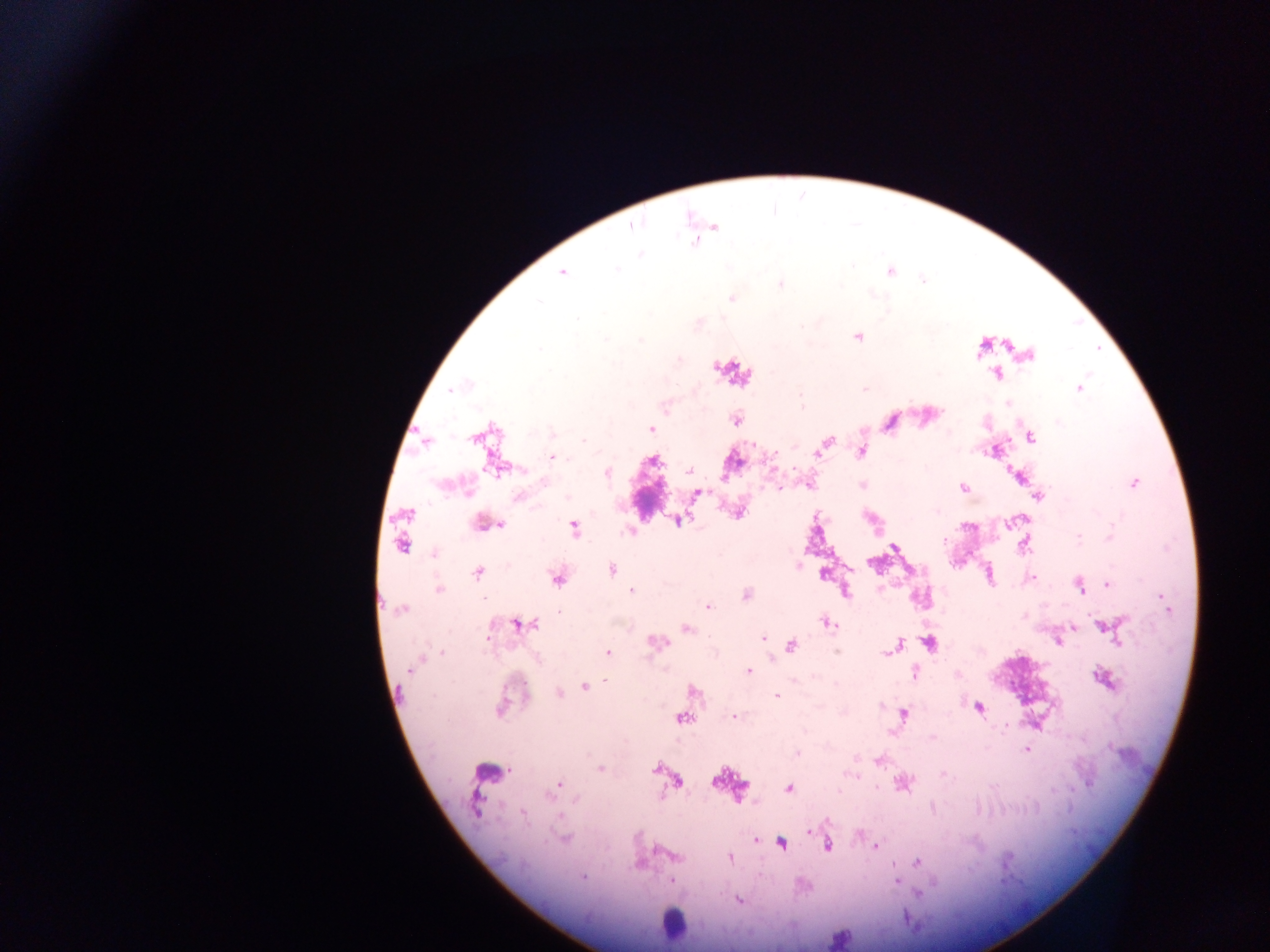
Approximate centers as [x, y] in pixels.
Summary:
  - Leukocyte locations: [733, 371], [484, 771], [673, 923], [839, 939]
  - Plasmodium parasite locations: [633, 226], [695, 243], [641, 255], [617, 270], [889, 272], [562, 273], [780, 284], [731, 298], [538, 301], [578, 318], [801, 326], [857, 336], [605, 339], [640, 341], [539, 349], [1029, 355], [995, 374], [455, 388], [864, 389], [1079, 389], [800, 397], [1007, 404], [735, 420], [1058, 422], [651, 429], [552, 434], [1031, 437], [476, 438], [584, 440], [425, 441], [825, 444], [753, 445], [820, 451], [861, 451], [775, 454], [554, 457], [654, 460], [499, 468], [690, 471], [607, 473], [1133, 483], [810, 486], [861, 486], [963, 488], [779, 489], [697, 494], [1039, 496], [518, 497], [567, 497], [407, 514], [679, 520], [1008, 523], [484, 524], [495, 525], [575, 528], [629, 531], [1110, 536], [1078, 538], [945, 541], [402, 544], [1023, 545], [893, 548], [434, 554], [798, 565], [612, 569], [478, 572], [1032, 577], [557, 579], [1108, 584], [1080, 587], [439, 589], [632, 591], [847, 593], [746, 595], [708, 607], [400, 610], [826, 622], [518, 624], [535, 624], [1105, 627], [686, 628], [1114, 633], [763, 637], [657, 642], [1059, 642], [929, 643], [791, 646], [898, 646], [891, 649], [836, 651], [442, 652], [608, 652], [886, 652], [418, 662], [414, 665], [748, 671], [915, 673], [1104, 679], [585, 686], [693, 691], [560, 693], [776, 696], [979, 708], [499, 709], [904, 714], [733, 716], [681, 718], [1006, 726], [933, 737], [1027, 749], [797, 753], [879, 761], [601, 769], [656, 769], [944, 774], [716, 780], [678, 782], [557, 786], [789, 788], [551, 791], [839, 791], [575, 799], [475, 805], [523, 813], [809, 831], [755, 839], [564, 840], [781, 843], [827, 846], [875, 847], [677, 856], [731, 858], [917, 862], [583, 878], [671, 881], [897, 882], [739, 900]
  - Preparation: thick blood smear
  - Capture: mobile-phone photograph through a microscope
  - Country: Ghana
  - Image size: 1270×952 pixels
  - Field of view: single